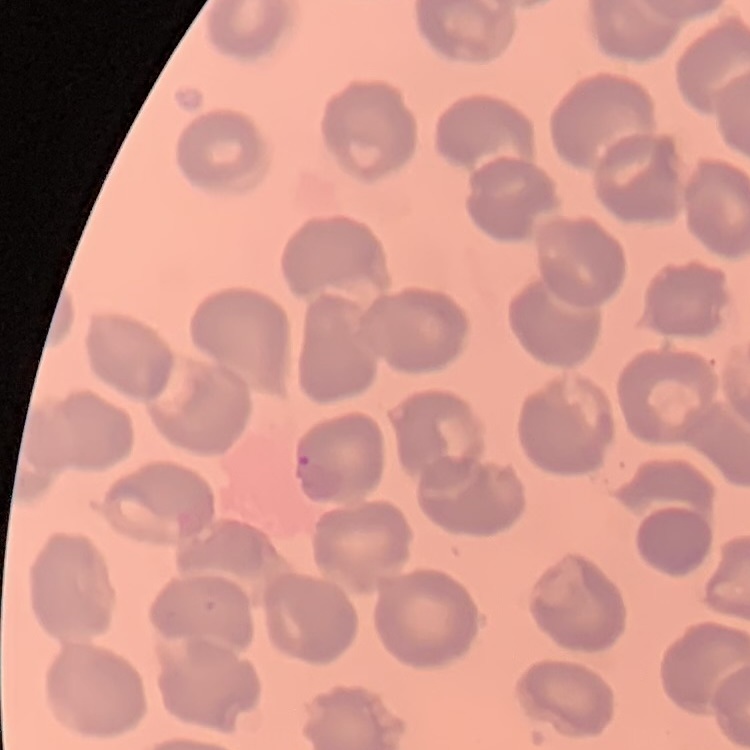

red blood cell morphology = no rouleaux formation
stain = Field's or Giemsa
image type = one tile cut from a larger photomicrograph
preparation = thin peripheral smear